Assess this cell for malaria.
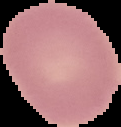

It is uninfected.

Summary:
  - Image size: 121×127 pixels
  - Image type: segmented cell region with the area outside set to black
  - Preparation: thin blood film